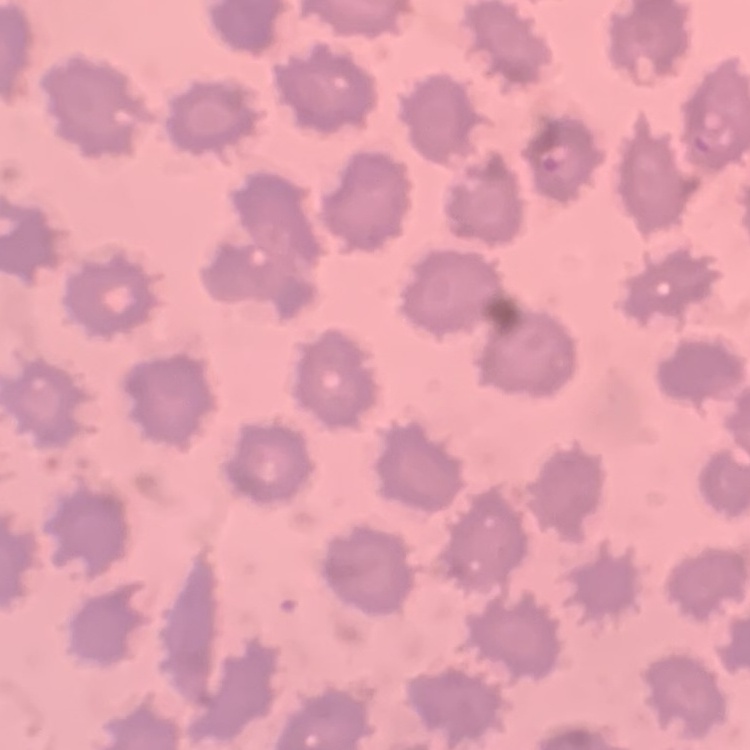

Summary:
  - Red blood cell morphology: no rouleaux formation
  - Image type: square crop of a larger photomicrograph
  - Preparation: thin blood smear
  - Stain: Field's or Giemsa